Describe the morphology of the red blood cells.
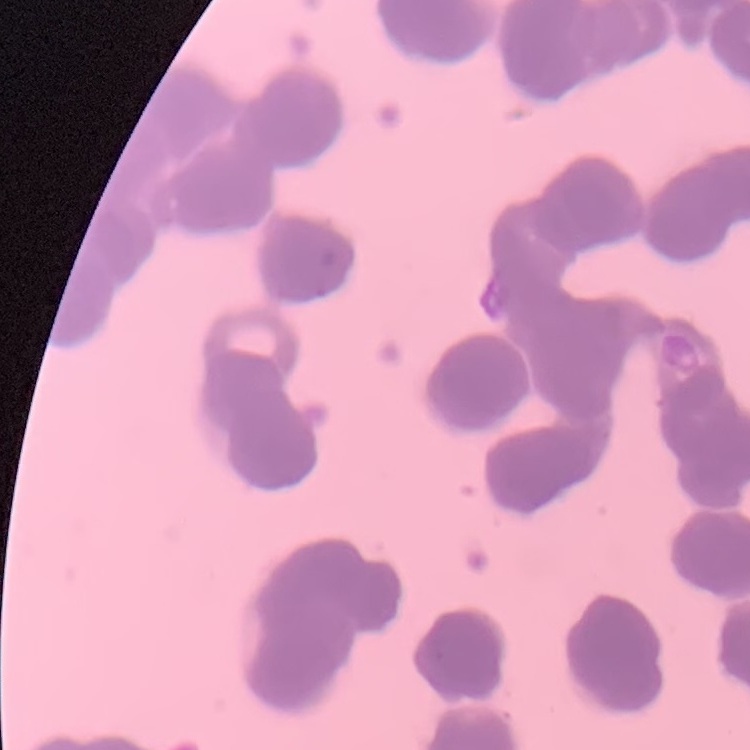

They show rouleaux formation.

Summary:
  - Image type: square crop of a larger photomicrograph
  - Preparation: thin peripheral smear
  - Stain: Field's or Giemsa